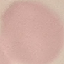
malaria_status: uninfected
preparation: thin smear
image_type: cell patch, automatically extracted from a larger field of view and resized to 64 × 64 pixels
stain: Giemsa
capture: smartphone camera at the microscope eyepiece